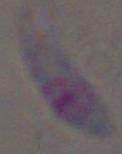
Captured at 1000x magnification. Micrograph. Toxoplasma gondii is shown.